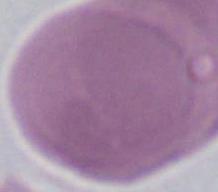
Summary:
  - Magnification: 1000x
  - Identification: erythrocyte
  - Modality: photomicrograph